Classify this cell by malaria status.
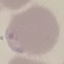
Parasitized.

{
  "preparation": "thin blood film",
  "image_type": "cell patch, automatically extracted from a larger field of view and resized to 64 × 64 pixels",
  "stain": "Giemsa",
  "capture": "smartphone through the microscope eyepiece"
}